Identify the parasite.
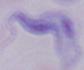

A trypanosome.

modality: photomicrograph
magnification: 1000x